Classify this cell by malaria status.
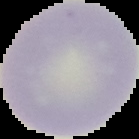
It is uninfected.

{
  "preparation": "thin blood film",
  "image_size": "139×139 pixels",
  "image_type": "segmented cell region on a black background"
}